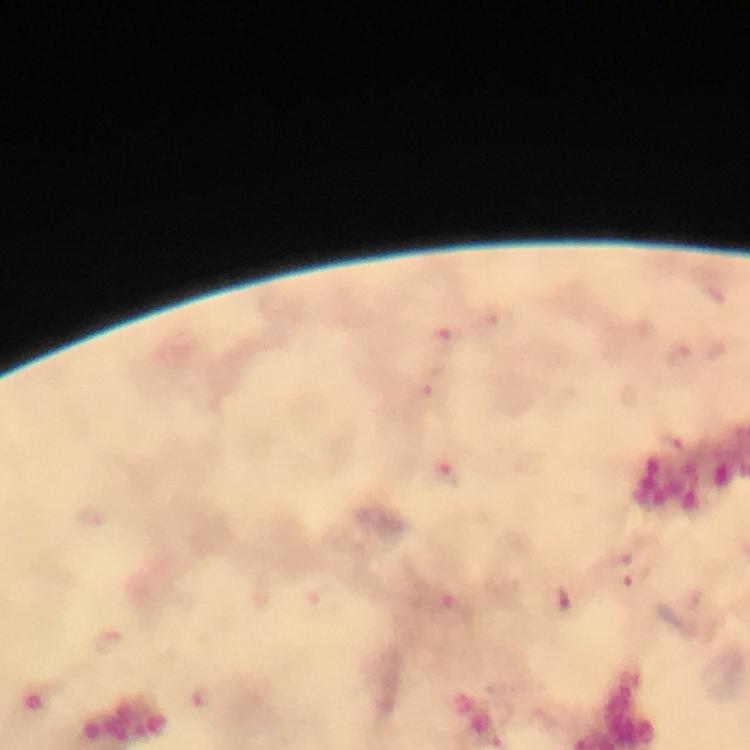

Approximate object centers, in pixels from the top-left corner. Malaria parasite locations: (x=498, y=319), (x=444, y=337), (x=680, y=358), (x=429, y=387), (x=446, y=473), (x=620, y=558), (x=635, y=579), (x=452, y=606), (x=108, y=641), (x=202, y=697). At 100x magnification. Cropped region of a single field of view. Photographed with a smartphone mounted on the microscope. From a diagnostic examination for malaria. Image is 750×750 pixels. Thick blood film. Giemsa-stained preparation. Immersion oil was used.